Locate every blood parasite and identify its species.
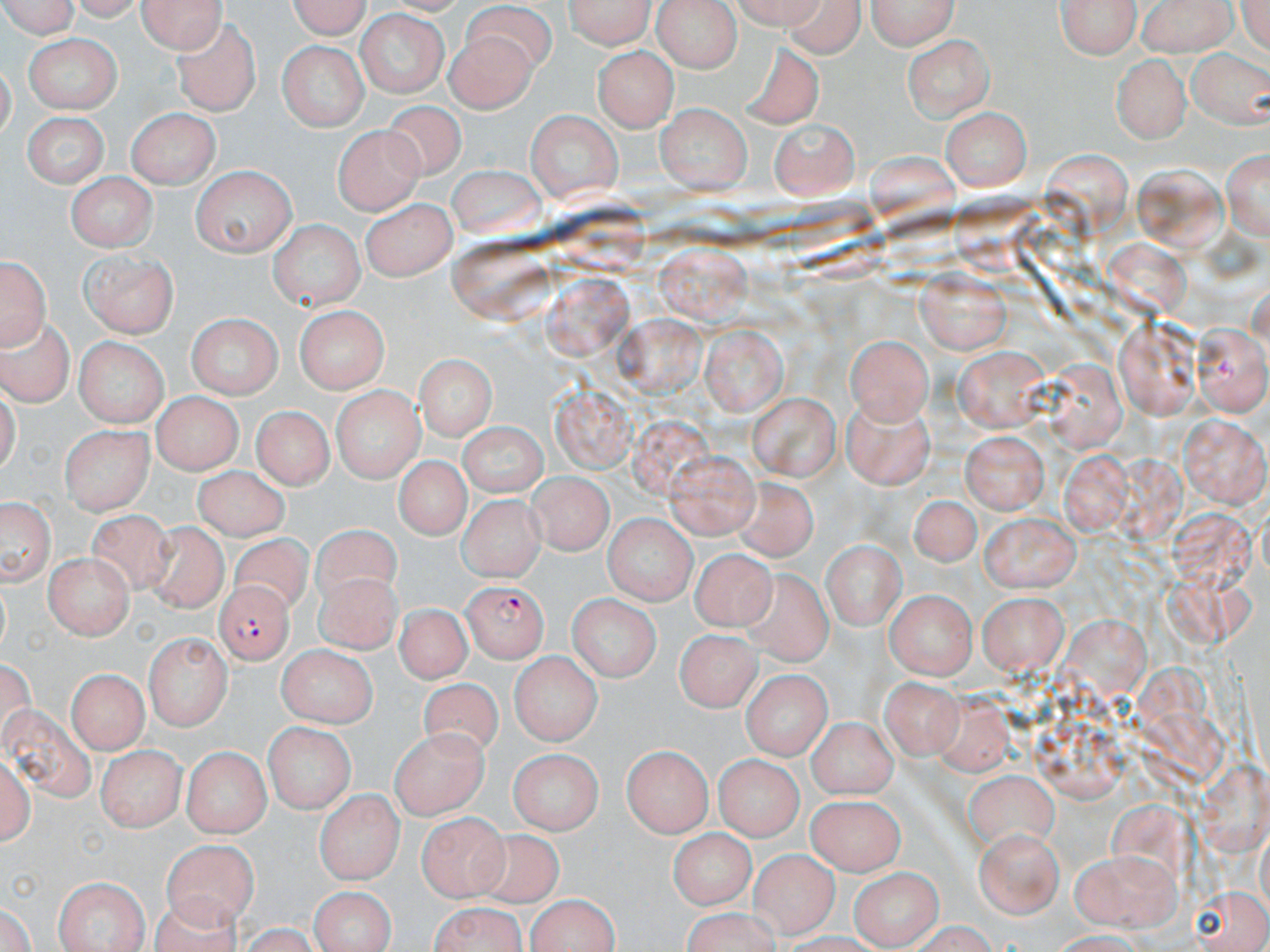
Approximate bounding boxes as named x1/y1/x2/y2 corners in pixels.
Plasmodium falciparum-infected red blood cells: (x1=461, y1=578, x2=550, y2=663), (x1=213, y1=581, x2=294, y2=666).
No Plasmodium ovale, Plasmodium malariae, Plasmodium vivax, Babesia divergens, or Trypanosoma brucei observed.

Uninfected red blood cell locations: (x1=0, y1=0, x2=86, y2=37), (x1=136, y1=0, x2=226, y2=53), (x1=281, y1=0, x2=372, y2=39), (x1=566, y1=0, x2=654, y2=49), (x1=779, y1=0, x2=866, y2=56), (x1=863, y1=0, x2=960, y2=49), (x1=1055, y1=0, x2=1140, y2=61), (x1=1138, y1=0, x2=1237, y2=56), (x1=652, y1=1, x2=745, y2=74), (x1=802, y1=2, x2=936, y2=53), (x1=461, y1=3, x2=560, y2=73), (x1=354, y1=12, x2=449, y2=98), (x1=573, y1=14, x2=660, y2=96), (x1=173, y1=19, x2=261, y2=117), (x1=441, y1=26, x2=539, y2=107), (x1=904, y1=34, x2=995, y2=121), (x1=25, y1=36, x2=119, y2=111), (x1=275, y1=41, x2=368, y2=133), (x1=740, y1=41, x2=826, y2=125), (x1=915, y1=44, x2=1016, y2=169), (x1=593, y1=45, x2=680, y2=129), (x1=1188, y1=46, x2=1270, y2=130), (x1=1110, y1=52, x2=1189, y2=142), (x1=382, y1=100, x2=471, y2=182), (x1=653, y1=104, x2=750, y2=193), (x1=127, y1=106, x2=221, y2=189), (x1=940, y1=107, x2=1030, y2=189), (x1=526, y1=110, x2=623, y2=203), (x1=19, y1=111, x2=109, y2=187), (x1=773, y1=116, x2=859, y2=195), (x1=336, y1=126, x2=425, y2=214), (x1=1224, y1=144, x2=1270, y2=244), (x1=443, y1=164, x2=545, y2=236), (x1=189, y1=167, x2=297, y2=256), (x1=64, y1=174, x2=157, y2=250), (x1=361, y1=199, x2=456, y2=281), (x1=270, y1=219, x2=364, y2=308), (x1=653, y1=241, x2=749, y2=326), (x1=79, y1=250, x2=180, y2=337), (x1=1, y1=251, x2=50, y2=347), (x1=917, y1=268, x2=1010, y2=357), (x1=292, y1=303, x2=391, y2=391), (x1=186, y1=313, x2=281, y2=399), (x1=0, y1=315, x2=75, y2=404), (x1=1115, y1=318, x2=1203, y2=416), (x1=700, y1=325, x2=787, y2=414), (x1=1188, y1=325, x2=1267, y2=415), (x1=846, y1=332, x2=936, y2=423), (x1=72, y1=335, x2=170, y2=426), (x1=950, y1=347, x2=1052, y2=433), (x1=414, y1=355, x2=495, y2=439), (x1=330, y1=386, x2=423, y2=481), (x1=150, y1=391, x2=240, y2=474), (x1=747, y1=391, x2=841, y2=481), (x1=839, y1=395, x2=939, y2=488), (x1=249, y1=405, x2=335, y2=488), (x1=1176, y1=417, x2=1270, y2=503), (x1=459, y1=419, x2=546, y2=499), (x1=61, y1=426, x2=153, y2=516), (x1=961, y1=430, x2=1046, y2=513), (x1=666, y1=450, x2=763, y2=537), (x1=390, y1=457, x2=470, y2=545), (x1=190, y1=465, x2=288, y2=538), (x1=526, y1=470, x2=612, y2=557), (x1=737, y1=475, x2=820, y2=562), (x1=908, y1=492, x2=982, y2=566), (x1=0, y1=494, x2=55, y2=590), (x1=455, y1=494, x2=547, y2=580), (x1=80, y1=509, x2=178, y2=601), (x1=982, y1=509, x2=1080, y2=589), (x1=604, y1=513, x2=697, y2=605), (x1=140, y1=520, x2=225, y2=621), (x1=301, y1=524, x2=400, y2=609), (x1=981, y1=526, x2=1078, y2=667), (x1=228, y1=531, x2=313, y2=612), (x1=824, y1=538, x2=904, y2=629), (x1=690, y1=549, x2=779, y2=629), (x1=43, y1=552, x2=133, y2=638), (x1=314, y1=571, x2=399, y2=652), (x1=733, y1=571, x2=835, y2=668), (x1=884, y1=589, x2=976, y2=679), (x1=976, y1=591, x2=1067, y2=676), (x1=569, y1=593, x2=662, y2=683), (x1=391, y1=603, x2=471, y2=686), (x1=677, y1=627, x2=761, y2=712), (x1=143, y1=632, x2=231, y2=732), (x1=274, y1=645, x2=377, y2=725), (x1=692, y1=648, x2=822, y2=729), (x1=512, y1=651, x2=600, y2=743), (x1=69, y1=667, x2=147, y2=753), (x1=739, y1=668, x2=834, y2=757), (x1=878, y1=672, x2=968, y2=769), (x1=419, y1=678, x2=503, y2=770), (x1=2, y1=697, x2=96, y2=812), (x1=808, y1=716, x2=899, y2=797), (x1=261, y1=721, x2=355, y2=811), (x1=390, y1=726, x2=488, y2=818), (x1=620, y1=743, x2=713, y2=838), (x1=182, y1=746, x2=270, y2=837), (x1=511, y1=747, x2=603, y2=832), (x1=1, y1=748, x2=32, y2=850), (x1=98, y1=748, x2=182, y2=832), (x1=711, y1=755, x2=802, y2=840), (x1=965, y1=765, x2=1057, y2=847), (x1=317, y1=788, x2=401, y2=884), (x1=806, y1=792, x2=903, y2=873), (x1=418, y1=811, x2=507, y2=898), (x1=672, y1=830, x2=754, y2=908), (x1=973, y1=830, x2=1065, y2=920), (x1=460, y1=833, x2=568, y2=912), (x1=162, y1=834, x2=261, y2=927), (x1=1072, y1=848, x2=1179, y2=931), (x1=746, y1=850, x2=838, y2=940), (x1=848, y1=867, x2=938, y2=947), (x1=51, y1=875, x2=149, y2=952), (x1=306, y1=885, x2=397, y2=951), (x1=523, y1=892, x2=624, y2=951), (x1=424, y1=899, x2=531, y2=952). Slide-level diagnosis: Plasmodium falciparum. Thin blood smear. Light microscopy. Single field of view. Image is 1270×952 pixels. May-Grünwald-Giemsa stain. Captured at 1000x magnification.